Report the malaria status of this cell.
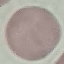
It is uninfected.

Automatically extracted cell patch, resized to 64 × 64 pixels. Thin blood film. Giemsa stain. Photographed with a smartphone camera at the microscope eyepiece.